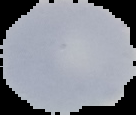 Malaria status: uninfected. From a thin blood film. Image is 136×115 pixels. The area outside the segmented cell region is set to black.